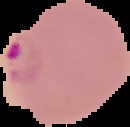
malaria_status: parasitized
image_size: 130×127 pixels
image_type: segmented cell region on a black background
preparation: thin blood film